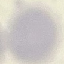

Summary:
  - Malaria status: uninfected
  - Preparation: thin blood smear
  - Capture: smartphone camera at the microscope eyepiece
  - Image type: automatically extracted cell patch, resized to 64 × 64 pixels
  - Stain: Giemsa